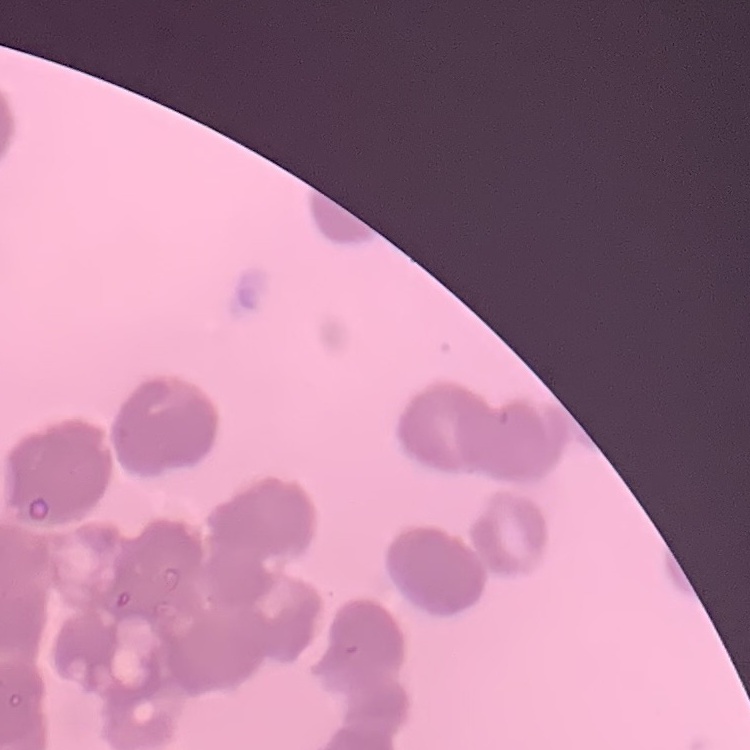
red blood cell morphology = rouleaux formation
stain = Field's or Giemsa
preparation = thin peripheral smear
image type = square crop of a larger photomicrograph